Describe the morphology of the erythrocytes.
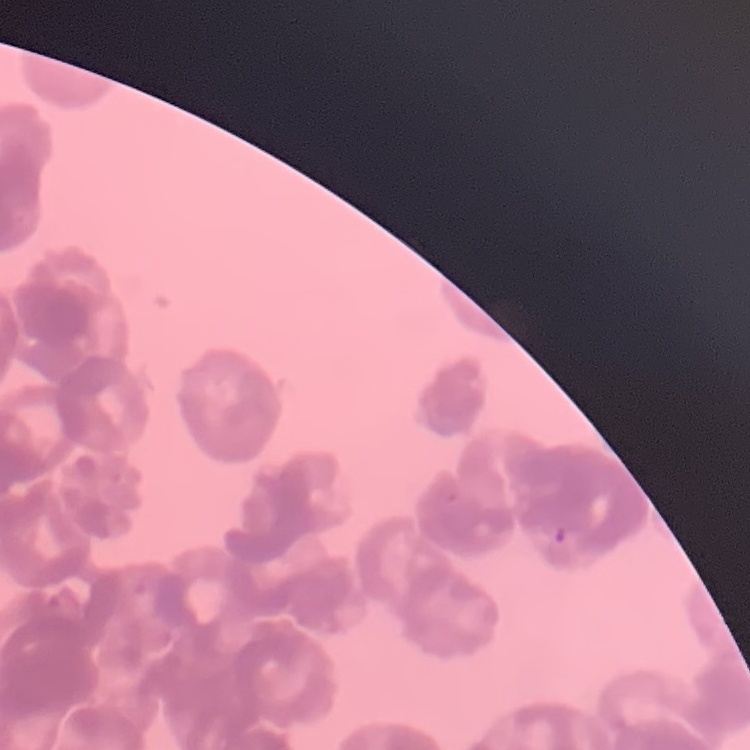
Rouleaux formation.

Thin blood smear. Field's or Giemsa stain. One tile cut from a larger photomicrograph.